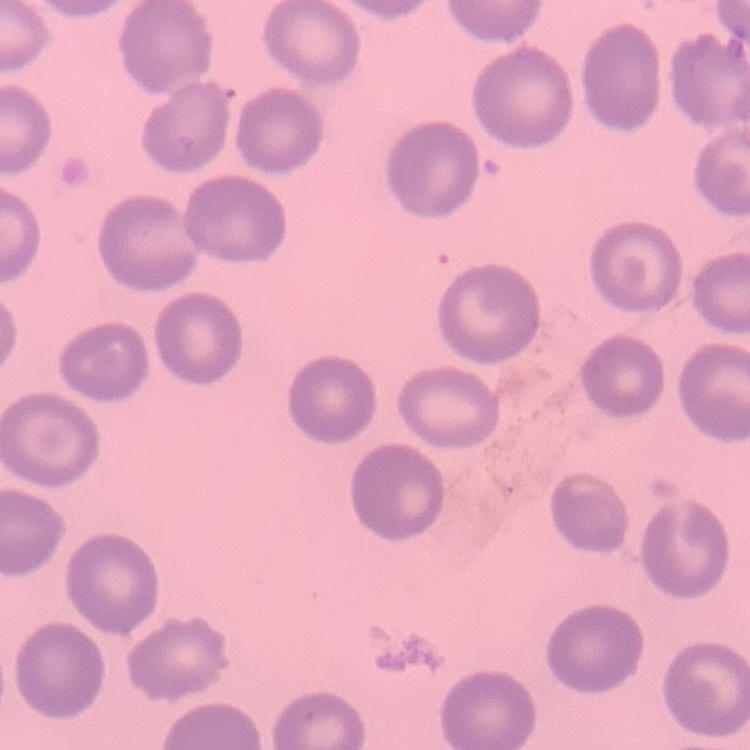

The erythrocytes show no rouleaux formation. Thin blood film. One tile cut from a larger photomicrograph. Field's or Giemsa stain.